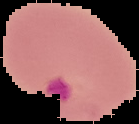
Summary:
  - Result: malaria parasites detected
  - Preparation: thin blood smear
  - Image size: 139×124 pixels
  - Image type: segmented cell region on a black background